Outline each blood parasite and name the species.
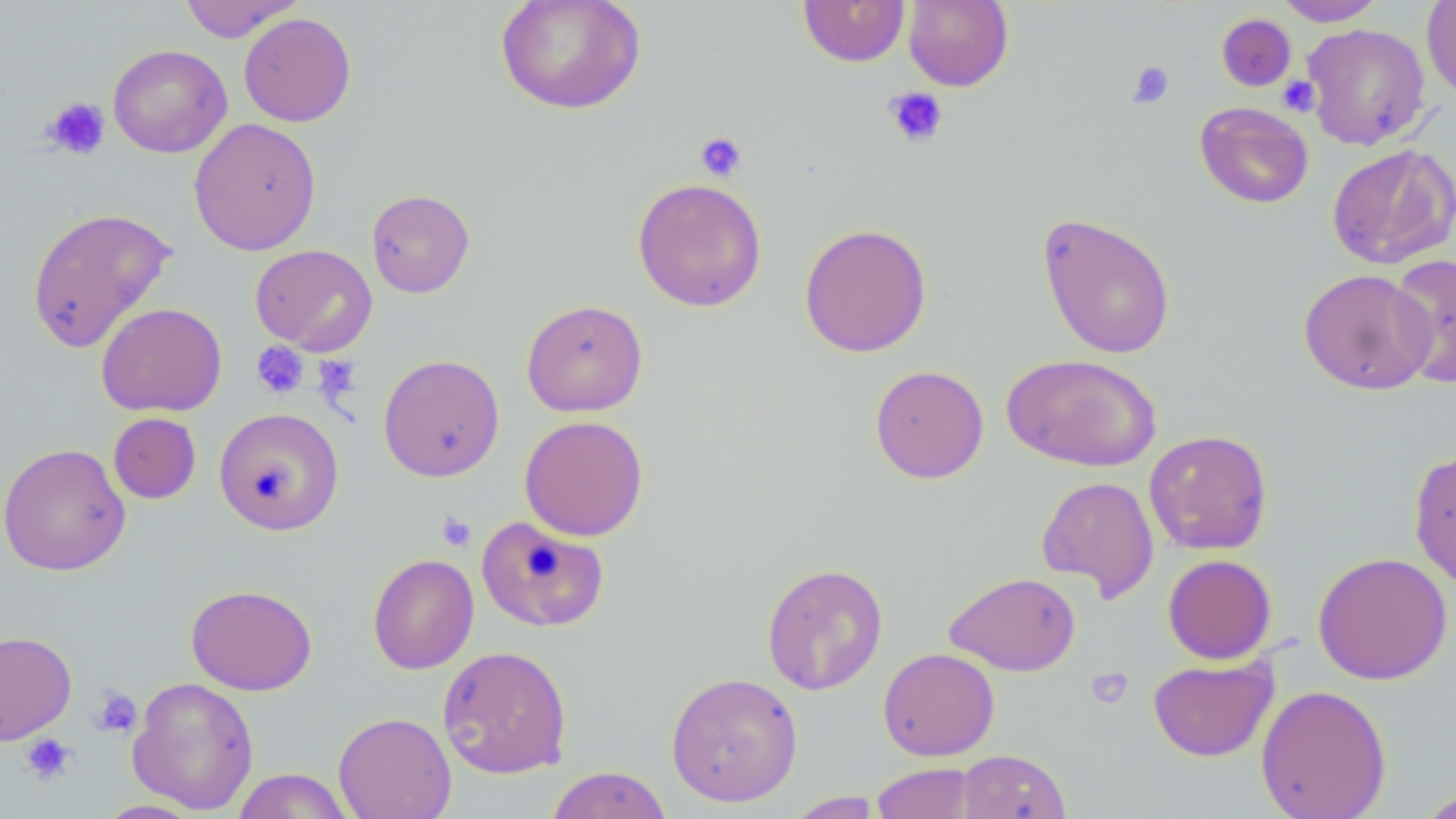
No blood parasites observed.

Summary:
  - Coordinate format: approximate bounding boxes as [x1, y1, x2, y2] in pixels
  - Uninfected red blood cell locations: [179, 0, 305, 42], [495, 0, 646, 115], [797, 0, 910, 67], [903, 0, 1014, 91], [1274, 0, 1387, 26], [1421, 0, 1456, 101], [238, 12, 356, 127], [1216, 13, 1297, 92], [1302, 23, 1431, 150], [107, 44, 232, 158], [1195, 101, 1314, 209], [188, 117, 322, 256], [1327, 143, 1456, 269], [632, 177, 767, 312], [366, 189, 475, 298], [25, 206, 178, 354], [1036, 211, 1177, 360], [798, 223, 932, 358], [250, 244, 377, 355], [1387, 252, 1455, 389], [1298, 268, 1436, 396], [521, 299, 648, 417], [96, 302, 227, 417], [378, 353, 505, 482], [1001, 354, 1162, 472], [869, 364, 990, 484], [214, 406, 345, 536], [108, 412, 201, 504], [519, 415, 649, 542], [1144, 429, 1273, 555], [0, 442, 131, 576], [1408, 447, 1456, 590], [1036, 475, 1160, 603], [475, 515, 610, 633], [1312, 551, 1453, 685], [367, 553, 479, 675], [1162, 554, 1277, 664], [761, 562, 888, 695], [945, 571, 1081, 676], [186, 584, 318, 695], [0, 630, 77, 744], [437, 645, 573, 779], [878, 647, 1000, 761], [1147, 656, 1278, 762], [665, 671, 803, 808], [127, 675, 259, 814], [1255, 684, 1392, 819], [333, 711, 457, 819], [956, 749, 1070, 819], [871, 762, 978, 819], [545, 765, 673, 819], [232, 768, 355, 819], [1415, 788, 1456, 819], [784, 791, 884, 818], [92, 799, 206, 818]
  - Platelet locations: [1126, 60, 1175, 109], [1278, 75, 1320, 116], [884, 86, 949, 149], [42, 96, 110, 159], [694, 131, 748, 182], [251, 340, 309, 400], [313, 355, 361, 404], [436, 511, 477, 552], [1085, 667, 1134, 710], [90, 687, 142, 738], [20, 732, 76, 786]
  - Slide-level diagnosis: negative for blood parasites
  - Field of view: single
  - Preparation: thin blood smear
  - Image size: 1456×819 pixels
  - Modality: light microscopy
  - Magnification: 1000x
  - Stain: May-Grünwald-Giemsa